Comment on the morphology of the red blood cells.
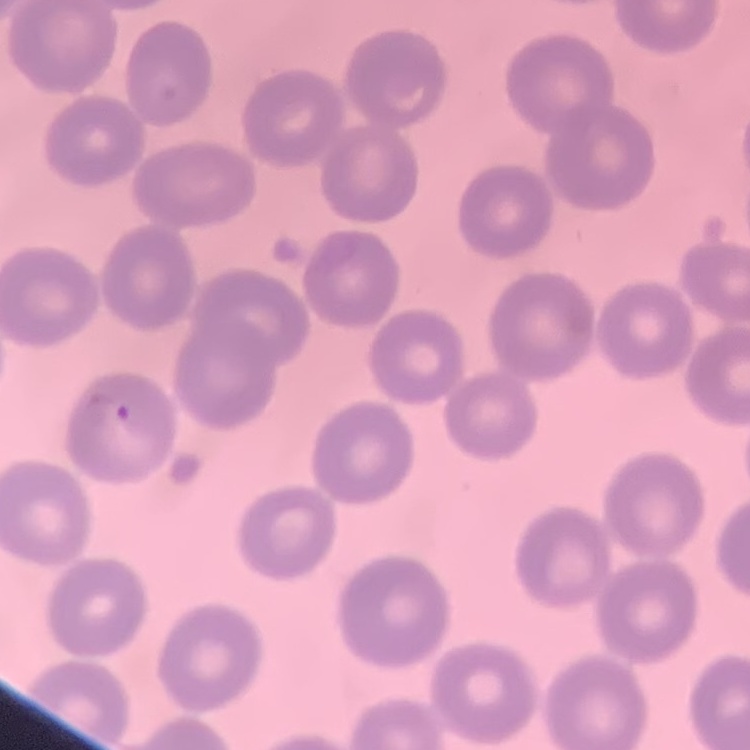
No rouleaux formation.

preparation = thin peripheral smear
stain = Field's or Giemsa
image type = square crop of a larger photomicrograph